Assess this cell for malaria.
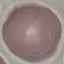

It is uninfected.

Automatically extracted cell patch, resized to 64 × 64 pixels. Thin blood smear. Acquired by smartphone through the microscope eyepiece. Giemsa-stained preparation.